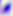 Captured at 400x magnification. Toxoplasma gondii is shown. Micrograph.